Identify the cell.
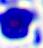

A leukocyte.

Micrograph. Captured at 400x magnification.